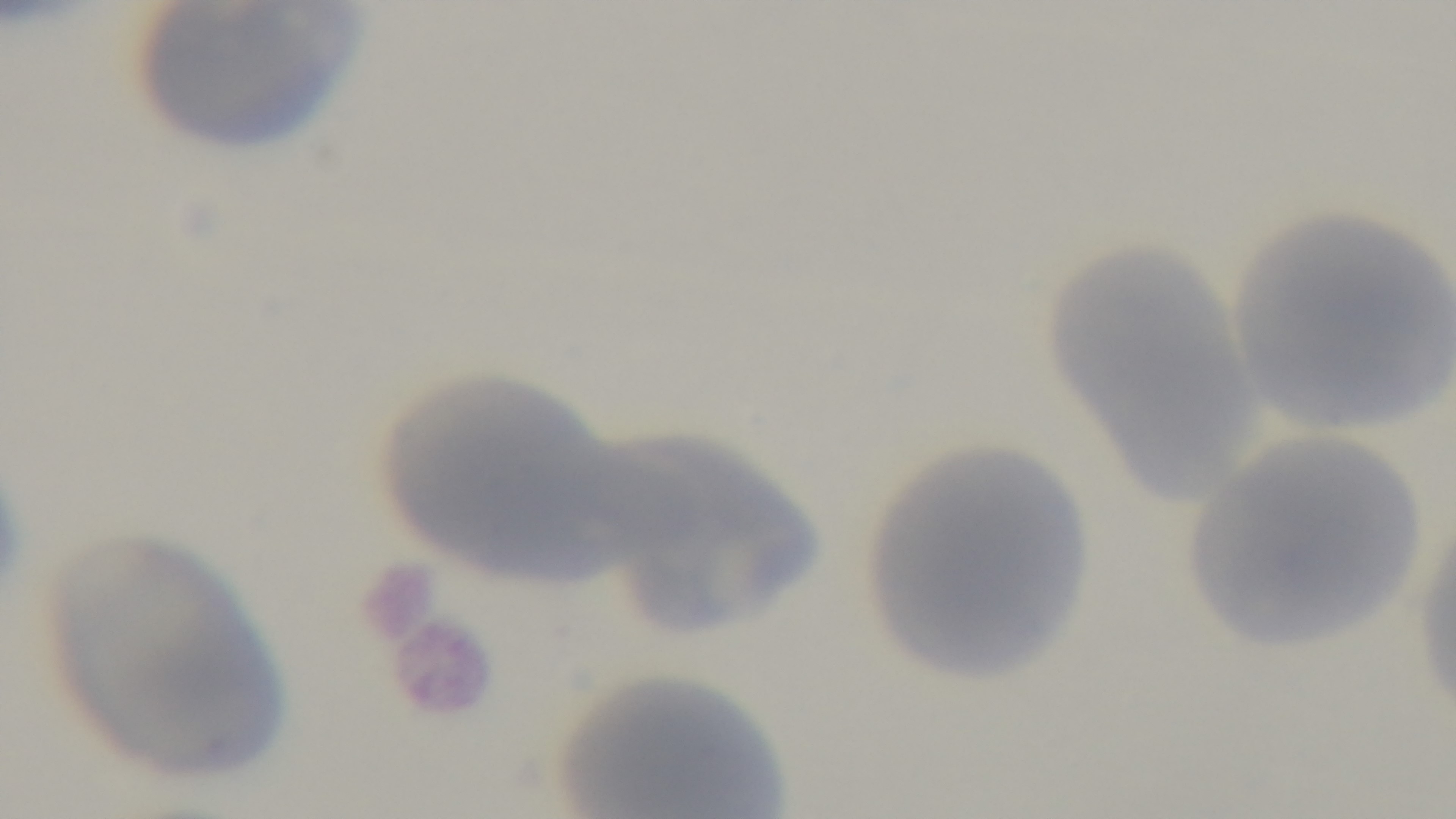

Summary:
  - Modality: light microscopy
  - Objective: 100x oil immersion
  - Field of view: one from the slide
  - Preparation: thin
  - Malaria status: negative
  - Stain: Giemsa
  - Capture: mounted 4K digital camera